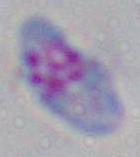

magnification = 1000x
modality = micrograph
identification = Toxoplasma gondii